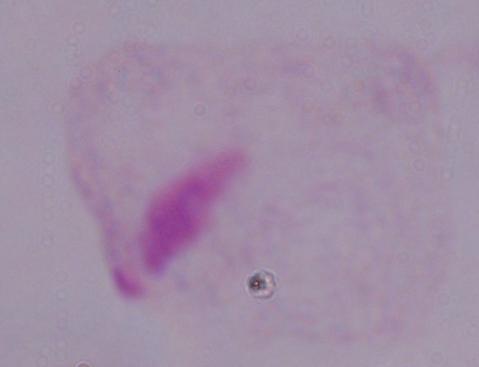

magnification = 1000x
modality = micrograph
identification = trichomonad